Point out each Plasmodium parasite.
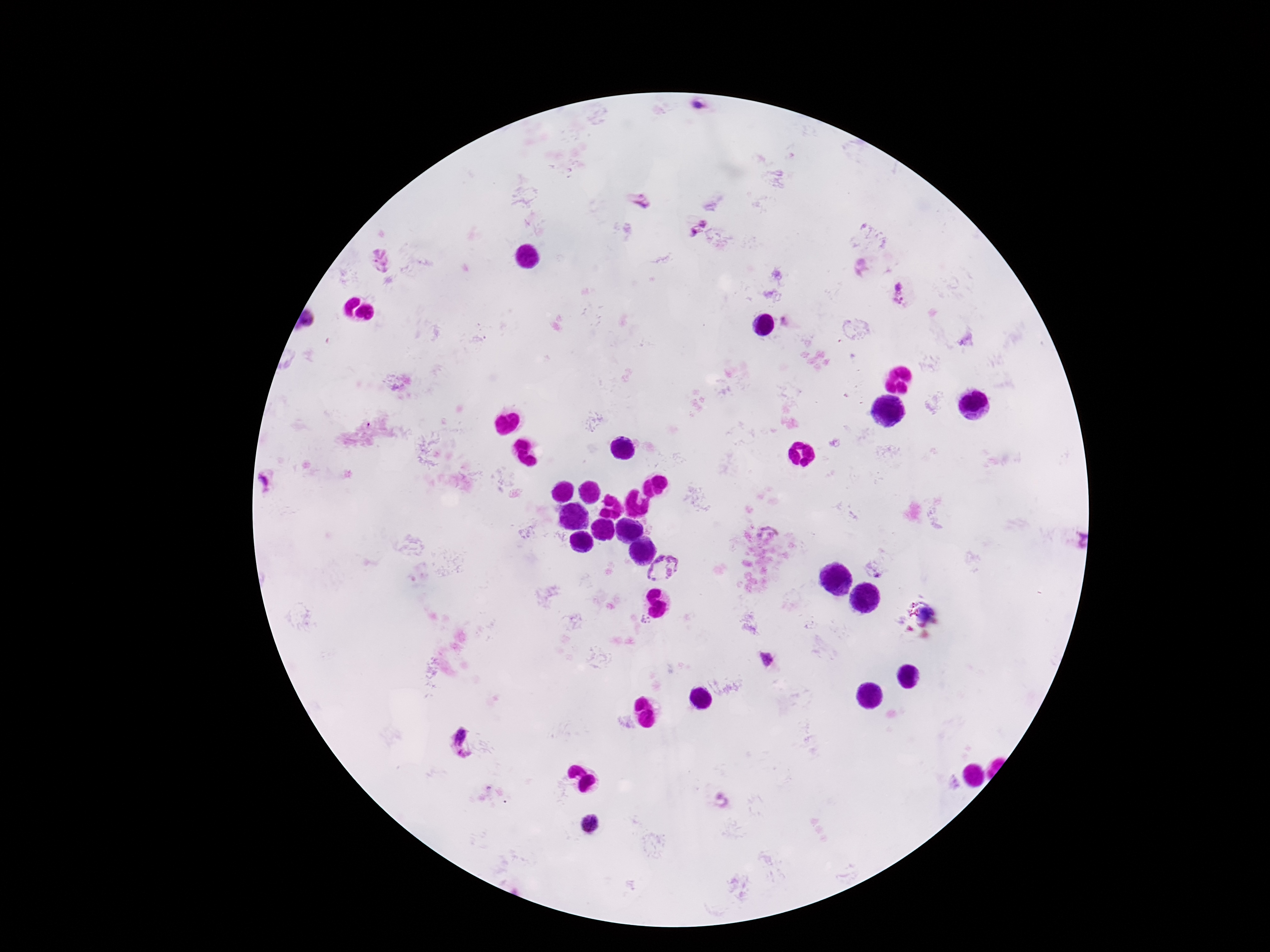
Approximate object centers, in pixels from the top-left corner.
Plasmodium parasites: (x=703, y=222), (x=696, y=232), (x=380, y=260), (x=901, y=292), (x=306, y=320), (x=769, y=532), (x=664, y=572), (x=767, y=657), (x=458, y=736), (x=463, y=755), (x=589, y=824).

Summary:
  - Magnification: 100x
  - Patient malaria status: infected
  - Capture: smartphone camera through the microscope eyepiece
  - Stain: Giemsa
  - Field of view: single
  - Image size: 1270×952 pixels
  - Preparation: thick blood film